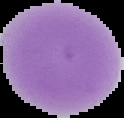
Malaria status: uninfected. From a thin blood film. Image is 124×118 pixels. The area outside the segmented cell region is set to black.